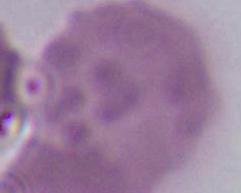

An erythrocyte is shown. Micrograph. 1000x magnification.